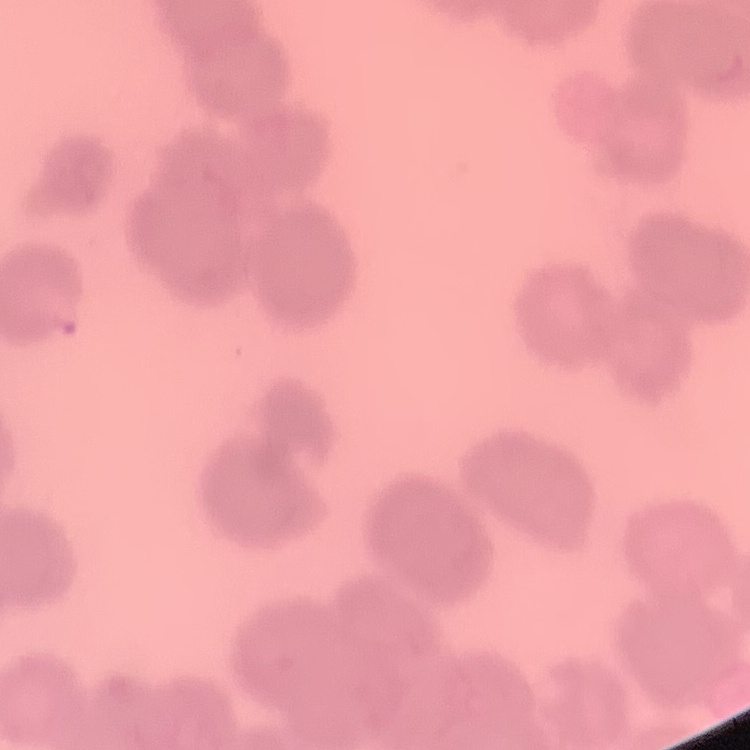
{
  "erythrocyte_morphology": "rouleaux formation",
  "preparation": "thin peripheral smear",
  "image_type": "one tile cut from a larger photomicrograph",
  "stain": "Field's or Giemsa"
}